Name the parasite shown.
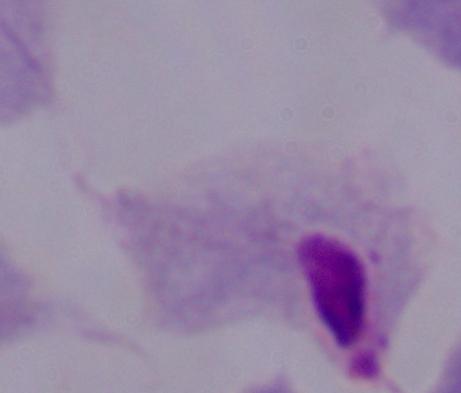
This is a trichomonad.

1000x magnification. Photomicrograph.